Locate every malaria parasite.
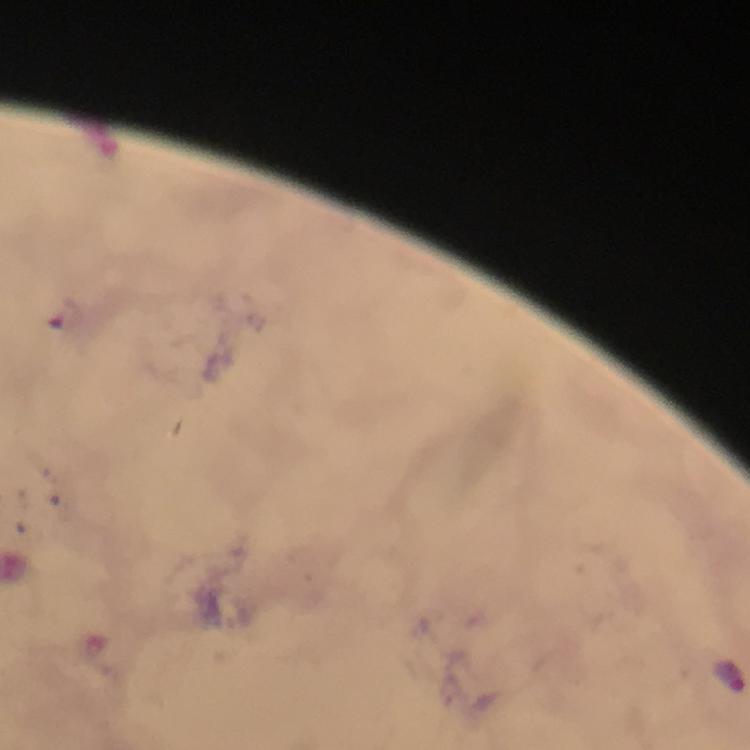
Approximate centers as {x, y} in pixels.
Malaria parasites: {727, 675}.

Summary:
  - Image size: 750×750 pixels
  - Stain: Giemsa
  - Context: from a malaria diagnostic workup
  - Cropped from: one field of view
  - Capture: smartphone mounted on the microscope
  - Immersion oil: applied
  - Preparation: thick smear
  - Magnification: 100x